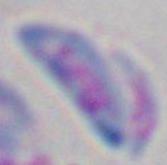

{
  "magnification": "1000x",
  "modality": "micrograph",
  "identification": "Toxoplasma gondii"
}